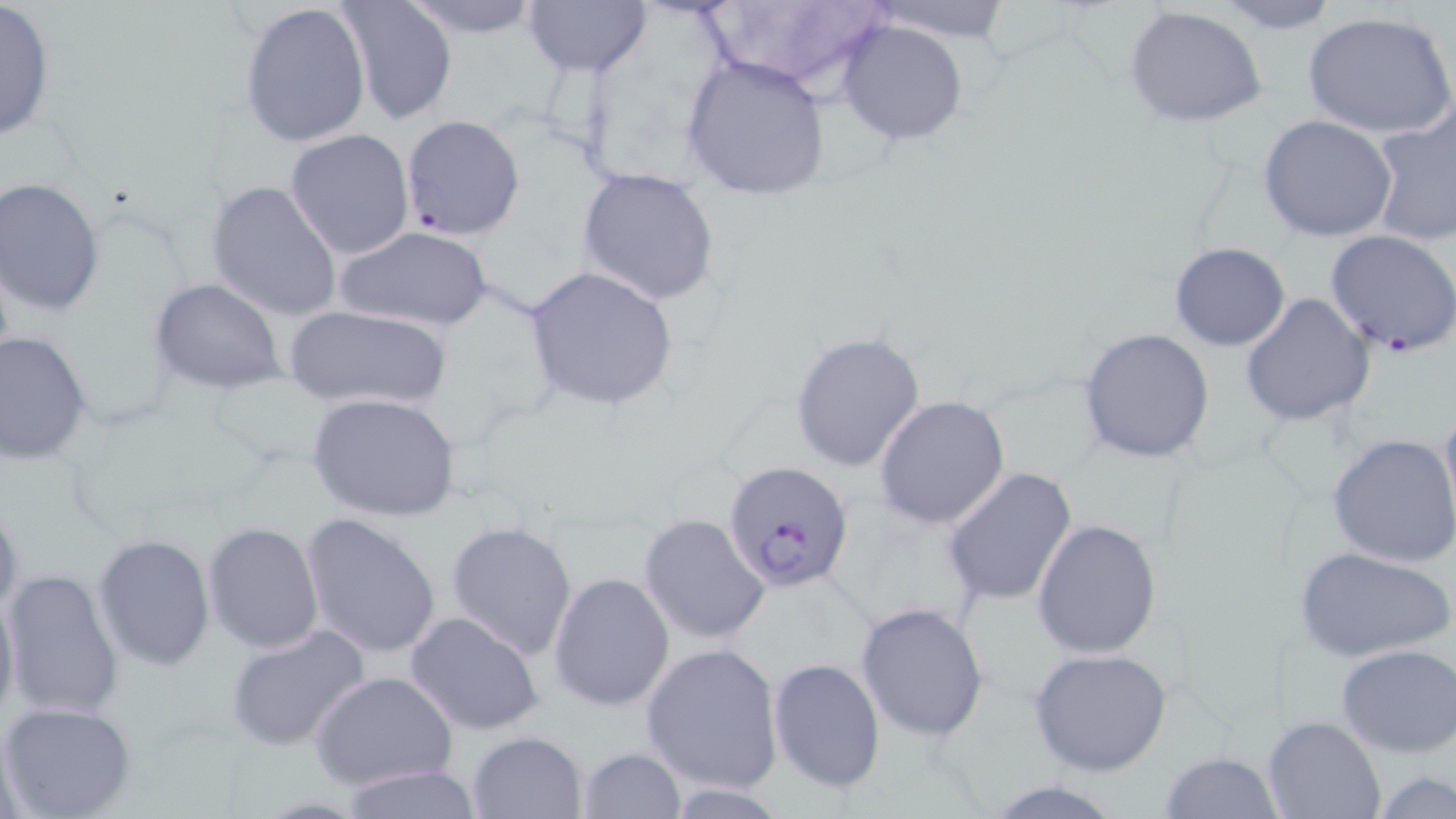

{
  "slide_level_diagnosis": "Plasmodium falciparum",
  "image_size": "1456×819 pixels",
  "uninfected_red_blood_cell_locations": "approximate bounding boxes as named x1/y1/x2/y2 corners in pixels: (x1=396, y1=0, x2=550, y2=38), (x1=521, y1=0, x2=654, y2=79), (x1=694, y1=0, x2=891, y2=97), (x1=861, y1=0, x2=1016, y2=44), (x1=1208, y1=0, x2=1344, y2=34), (x1=336, y1=1, x2=460, y2=125), (x1=238, y1=2, x2=372, y2=149), (x1=0, y1=3, x2=55, y2=142), (x1=1123, y1=6, x2=1269, y2=130), (x1=1301, y1=9, x2=1456, y2=142), (x1=835, y1=19, x2=970, y2=145), (x1=679, y1=54, x2=831, y2=201), (x1=1369, y1=106, x2=1456, y2=247), (x1=398, y1=114, x2=524, y2=241), (x1=1258, y1=115, x2=1399, y2=243), (x1=286, y1=128, x2=414, y2=259), (x1=576, y1=166, x2=719, y2=305), (x1=0, y1=178, x2=104, y2=314), (x1=205, y1=179, x2=344, y2=323), (x1=328, y1=225, x2=496, y2=333), (x1=1324, y1=229, x2=1456, y2=356), (x1=1169, y1=242, x2=1290, y2=351), (x1=523, y1=266, x2=679, y2=411), (x1=150, y1=275, x2=284, y2=395), (x1=1240, y1=293, x2=1373, y2=428), (x1=286, y1=305, x2=453, y2=413), (x1=1078, y1=327, x2=1216, y2=464), (x1=0, y1=331, x2=94, y2=463), (x1=790, y1=331, x2=927, y2=473), (x1=306, y1=392, x2=461, y2=523), (x1=873, y1=394, x2=1010, y2=530), (x1=1438, y1=399, x2=1456, y2=537), (x1=1327, y1=433, x2=1456, y2=567), (x1=940, y1=467, x2=1078, y2=609), (x1=0, y1=498, x2=24, y2=624), (x1=298, y1=512, x2=443, y2=659), (x1=638, y1=513, x2=769, y2=644), (x1=1030, y1=518, x2=1162, y2=657), (x1=202, y1=521, x2=325, y2=653), (x1=445, y1=521, x2=578, y2=660), (x1=92, y1=534, x2=215, y2=671), (x1=1294, y1=547, x2=1453, y2=662), (x1=2, y1=570, x2=125, y2=720), (x1=549, y1=572, x2=675, y2=711), (x1=0, y1=581, x2=19, y2=725), (x1=855, y1=601, x2=990, y2=741), (x1=403, y1=611, x2=548, y2=736), (x1=225, y1=625, x2=370, y2=751), (x1=640, y1=642, x2=784, y2=796), (x1=1335, y1=644, x2=1456, y2=757), (x1=1028, y1=647, x2=1173, y2=777), (x1=768, y1=657, x2=885, y2=794), (x1=311, y1=672, x2=457, y2=790), (x1=0, y1=701, x2=137, y2=818), (x1=1263, y1=715, x2=1384, y2=819), (x1=466, y1=730, x2=587, y2=818), (x1=575, y1=747, x2=687, y2=819), (x1=1159, y1=750, x2=1285, y2=819), (x1=331, y1=764, x2=485, y2=819), (x1=1374, y1=772, x2=1455, y2=817), (x1=978, y1=779, x2=1133, y2=819)",
  "modality": "light microscopy",
  "stain": "May-Grünwald-Giemsa",
  "magnification": "1000x",
  "field_of_view": "single",
  "plasmodium_falciparum_infected_red_blood_cell_locations": "approximate bounding boxes as named x1/y1/x2/y2 corners in pixels: (x1=722, y1=461, x2=855, y2=593)",
  "preparation": "thin blood smear"
}